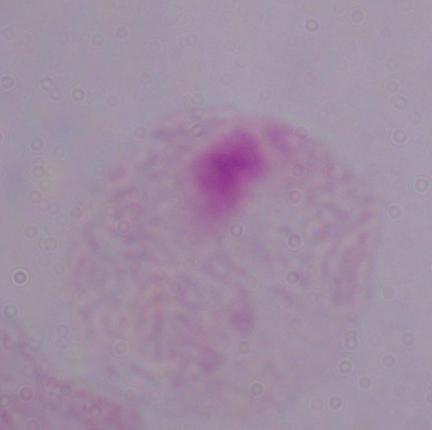

modality = micrograph
magnification = 1000x
identification = trichomonad